State which parasite is depicted.
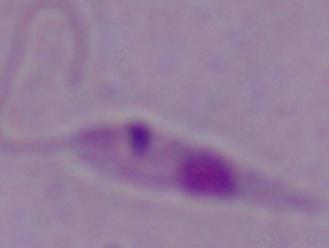

This is Leishmania.

magnification: 1000x
modality: micrograph